State which cell type is depicted.
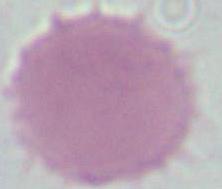
This is an erythrocyte.

magnification = 1000x
modality = photomicrograph